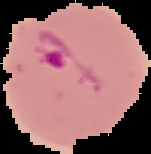
Summary:
  - Image size: 151×154 pixels
  - Image type: cell region segmented out of the field of view; surrounding area masked to black
  - Preparation: thin blood smear
  - Malaria status: parasitized